Identify the blood parasite species.
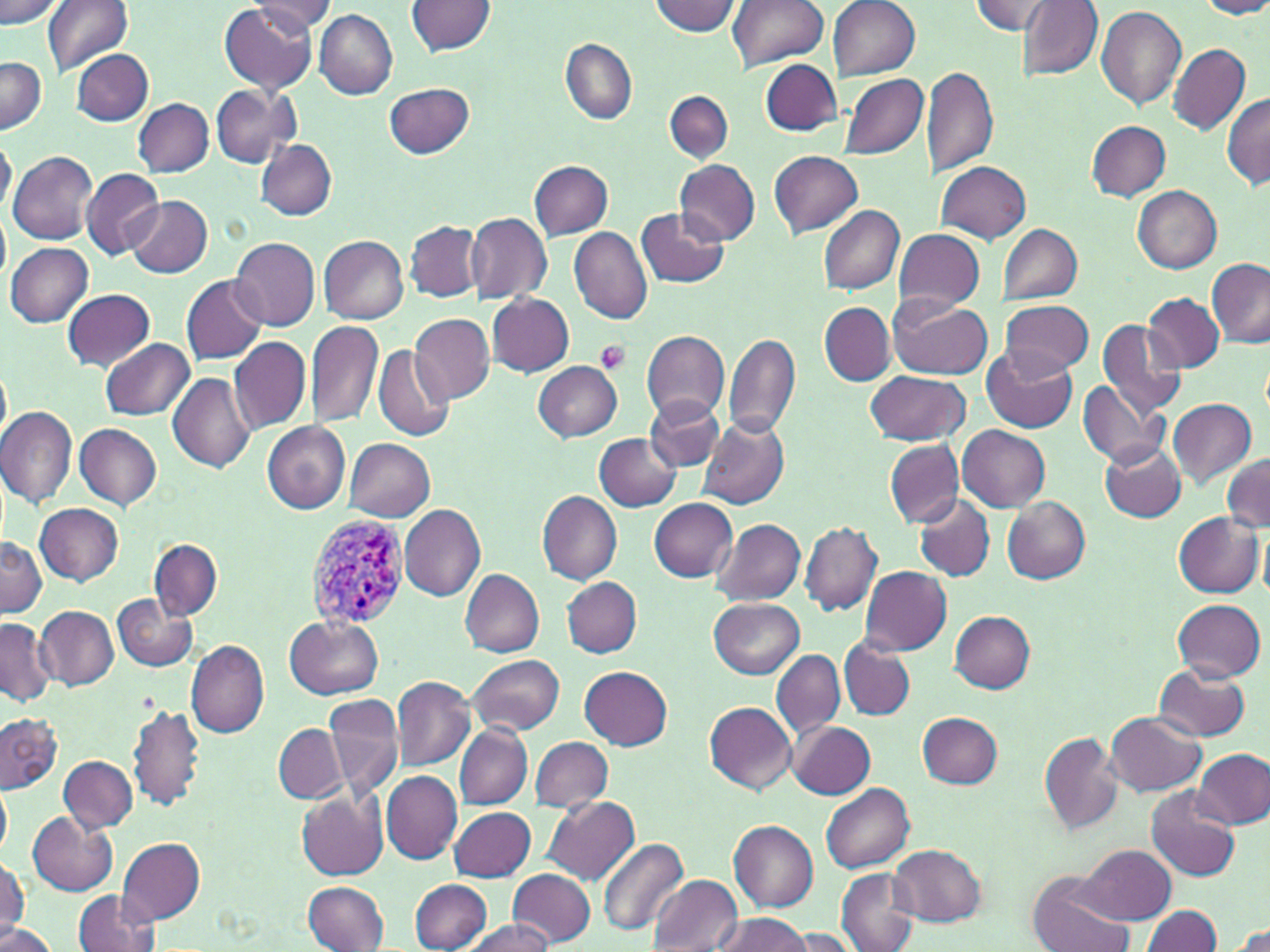

Plasmodium vivax.

Approximate bounding boxes as named x1/y1/x2/y2 corners in pixels. Plasmodium vivax-infected red blood cell locations: (x1=304, y1=515, x2=409, y2=630). Platelet locations: (x1=594, y1=341, x2=631, y2=373). Uninfected red blood cell locations: (x1=0, y1=0, x2=64, y2=26), (x1=42, y1=0, x2=133, y2=76), (x1=248, y1=0, x2=336, y2=34), (x1=649, y1=0, x2=740, y2=36), (x1=727, y1=0, x2=828, y2=71), (x1=831, y1=0, x2=921, y2=80), (x1=970, y1=0, x2=1052, y2=35), (x1=1196, y1=0, x2=1270, y2=19), (x1=1016, y1=1, x2=1103, y2=83), (x1=407, y1=2, x2=495, y2=55), (x1=218, y1=3, x2=319, y2=95), (x1=1094, y1=6, x2=1187, y2=110), (x1=313, y1=9, x2=399, y2=100), (x1=560, y1=39, x2=638, y2=125), (x1=1170, y1=44, x2=1250, y2=134), (x1=72, y1=50, x2=153, y2=124), (x1=0, y1=56, x2=46, y2=135), (x1=761, y1=59, x2=841, y2=134), (x1=922, y1=63, x2=997, y2=181), (x1=838, y1=72, x2=927, y2=163), (x1=384, y1=83, x2=476, y2=158), (x1=211, y1=86, x2=301, y2=169), (x1=665, y1=90, x2=733, y2=165), (x1=1222, y1=93, x2=1270, y2=189), (x1=133, y1=99, x2=213, y2=176), (x1=1087, y1=121, x2=1171, y2=201), (x1=0, y1=137, x2=16, y2=218), (x1=255, y1=139, x2=337, y2=221), (x1=9, y1=150, x2=99, y2=245), (x1=769, y1=151, x2=862, y2=239), (x1=676, y1=159, x2=760, y2=245), (x1=935, y1=160, x2=1031, y2=243), (x1=528, y1=161, x2=613, y2=238), (x1=80, y1=168, x2=163, y2=259), (x1=1132, y1=186, x2=1223, y2=273), (x1=127, y1=194, x2=212, y2=278), (x1=818, y1=205, x2=905, y2=293), (x1=637, y1=207, x2=730, y2=288), (x1=0, y1=211, x2=9, y2=284), (x1=465, y1=212, x2=552, y2=303), (x1=406, y1=220, x2=484, y2=303), (x1=567, y1=225, x2=654, y2=324), (x1=997, y1=225, x2=1082, y2=304), (x1=894, y1=228, x2=985, y2=310), (x1=229, y1=235, x2=320, y2=330), (x1=318, y1=235, x2=409, y2=324), (x1=6, y1=243, x2=94, y2=328), (x1=1207, y1=259, x2=1270, y2=347), (x1=182, y1=274, x2=267, y2=365), (x1=62, y1=289, x2=154, y2=370), (x1=487, y1=293, x2=573, y2=376), (x1=1142, y1=293, x2=1225, y2=373), (x1=889, y1=297, x2=993, y2=379), (x1=999, y1=300, x2=1092, y2=378), (x1=819, y1=303, x2=894, y2=385), (x1=409, y1=312, x2=496, y2=404), (x1=1097, y1=319, x2=1186, y2=416), (x1=306, y1=321, x2=383, y2=428), (x1=642, y1=331, x2=729, y2=422), (x1=722, y1=332, x2=799, y2=440), (x1=230, y1=336, x2=310, y2=433), (x1=101, y1=337, x2=196, y2=420), (x1=980, y1=343, x2=1077, y2=433), (x1=372, y1=344, x2=456, y2=442), (x1=534, y1=360, x2=622, y2=442), (x1=0, y1=361, x2=11, y2=448), (x1=865, y1=371, x2=968, y2=444), (x1=168, y1=373, x2=256, y2=473), (x1=1079, y1=380, x2=1168, y2=469), (x1=645, y1=396, x2=724, y2=471), (x1=1168, y1=398, x2=1256, y2=488), (x1=0, y1=407, x2=76, y2=506), (x1=698, y1=418, x2=789, y2=509), (x1=262, y1=420, x2=351, y2=513), (x1=75, y1=423, x2=161, y2=508), (x1=958, y1=426, x2=1050, y2=511), (x1=594, y1=432, x2=684, y2=512), (x1=345, y1=439, x2=435, y2=522), (x1=884, y1=440, x2=964, y2=527), (x1=1100, y1=441, x2=1187, y2=520), (x1=1220, y1=454, x2=1270, y2=534), (x1=536, y1=489, x2=621, y2=584), (x1=914, y1=494, x2=995, y2=583), (x1=649, y1=498, x2=736, y2=582), (x1=1003, y1=499, x2=1091, y2=583), (x1=35, y1=503, x2=123, y2=585), (x1=400, y1=503, x2=486, y2=601), (x1=1174, y1=510, x2=1264, y2=596), (x1=711, y1=519, x2=805, y2=607), (x1=800, y1=522, x2=881, y2=615), (x1=1260, y1=527, x2=1270, y2=603), (x1=0, y1=536, x2=45, y2=618), (x1=151, y1=538, x2=222, y2=621), (x1=859, y1=566, x2=951, y2=654), (x1=461, y1=569, x2=544, y2=656), (x1=563, y1=577, x2=642, y2=658), (x1=113, y1=595, x2=196, y2=672), (x1=710, y1=598, x2=804, y2=678), (x1=1172, y1=598, x2=1265, y2=683), (x1=35, y1=605, x2=117, y2=689), (x1=949, y1=610, x2=1035, y2=691), (x1=285, y1=616, x2=384, y2=699), (x1=0, y1=617, x2=53, y2=704), (x1=839, y1=637, x2=917, y2=721), (x1=185, y1=640, x2=270, y2=739), (x1=772, y1=651, x2=844, y2=740), (x1=467, y1=654, x2=565, y2=736), (x1=1154, y1=664, x2=1251, y2=742), (x1=581, y1=666, x2=672, y2=749), (x1=391, y1=676, x2=476, y2=772), (x1=323, y1=693, x2=404, y2=800), (x1=706, y1=702, x2=796, y2=793), (x1=129, y1=704, x2=205, y2=811), (x1=918, y1=712, x2=1004, y2=788), (x1=1105, y1=712, x2=1206, y2=796), (x1=0, y1=713, x2=64, y2=795), (x1=788, y1=720, x2=875, y2=798), (x1=274, y1=725, x2=346, y2=803), (x1=455, y1=726, x2=531, y2=809), (x1=1038, y1=732, x2=1123, y2=835), (x1=531, y1=737, x2=613, y2=811), (x1=1195, y1=749, x2=1269, y2=828), (x1=60, y1=755, x2=136, y2=832), (x1=380, y1=771, x2=461, y2=864), (x1=0, y1=782, x2=12, y2=858), (x1=820, y1=783, x2=915, y2=874), (x1=1146, y1=786, x2=1240, y2=883), (x1=296, y1=790, x2=387, y2=880), (x1=543, y1=796, x2=639, y2=884), (x1=449, y1=807, x2=535, y2=882), (x1=27, y1=809, x2=118, y2=895), (x1=728, y1=820, x2=818, y2=910), (x1=597, y1=836, x2=689, y2=937), (x1=119, y1=837, x2=205, y2=924), (x1=888, y1=844, x2=985, y2=925), (x1=1078, y1=844, x2=1174, y2=924), (x1=0, y1=855, x2=29, y2=937), (x1=507, y1=869, x2=596, y2=947), (x1=834, y1=870, x2=918, y2=951), (x1=1029, y1=872, x2=1135, y2=952), (x1=646, y1=874, x2=742, y2=952), (x1=409, y1=879, x2=492, y2=952), (x1=302, y1=881, x2=387, y2=951), (x1=72, y1=890, x2=161, y2=952), (x1=1141, y1=904, x2=1222, y2=952), (x1=711, y1=912, x2=810, y2=952), (x1=463, y1=918, x2=552, y2=952), (x1=1228, y1=920, x2=1270, y2=952), (x1=0, y1=923, x2=52, y2=952), (x1=787, y1=929, x2=862, y2=951). Image is 1270×952 pixels. Thin blood film. Single field of view. Light microscopy. 1000x magnification. May-Grünwald-Giemsa stain.